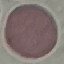

Summary:
  - Result: no malaria parasites detected
  - Image type: cell patch, automatically extracted from a larger field of view and resized to 64 × 64 pixels
  - Capture: smartphone camera at the microscope eyepiece
  - Preparation: thin blood film
  - Stain: Giemsa